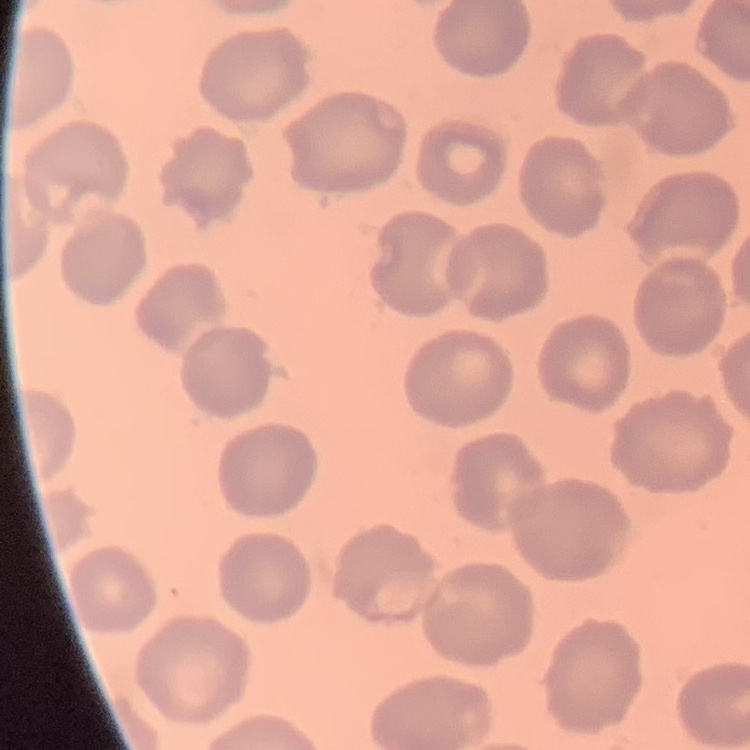

The erythrocytes show no rouleaux formation. Field's or Giemsa stain. Thin blood film. One tile cut from a larger photomicrograph.